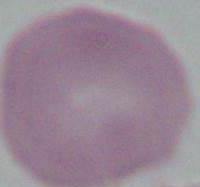
Micrograph. 1000x magnification. An erythrocyte is seen.